Locate and identify every blood parasite.
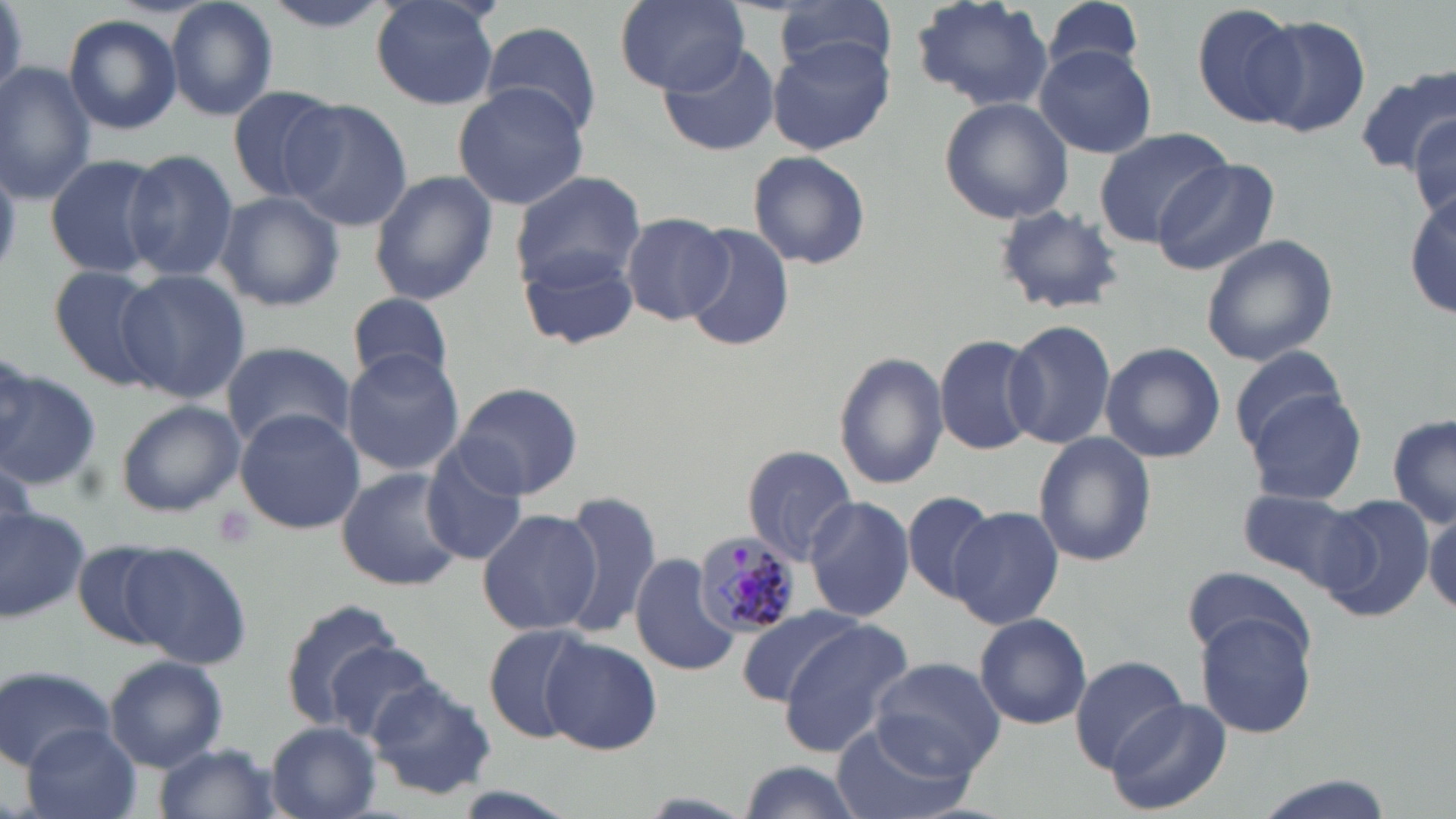

Approximate bounding boxes as named x1/y1/x2/y2 corners in pixels.
Plasmodium malariae-infected red blood cells: (x1=690, y1=529, x2=799, y2=639).
No Plasmodium falciparum, Plasmodium ovale, Plasmodium vivax, Babesia divergens, or Trypanosoma brucei observed.

Uninfected red blood cell locations: (x1=166, y1=0, x2=280, y2=120), (x1=252, y1=0, x2=401, y2=32), (x1=367, y1=0, x2=502, y2=109), (x1=611, y1=0, x2=752, y2=96), (x1=911, y1=0, x2=1053, y2=114), (x1=1038, y1=0, x2=1148, y2=82), (x1=772, y1=1, x2=901, y2=82), (x1=1190, y1=3, x2=1305, y2=128), (x1=64, y1=13, x2=183, y2=135), (x1=1253, y1=15, x2=1374, y2=139), (x1=478, y1=20, x2=604, y2=138), (x1=767, y1=37, x2=893, y2=153), (x1=659, y1=40, x2=782, y2=156), (x1=1035, y1=45, x2=1158, y2=158), (x1=0, y1=62, x2=97, y2=201), (x1=1353, y1=69, x2=1456, y2=181), (x1=452, y1=80, x2=590, y2=211), (x1=224, y1=84, x2=341, y2=203), (x1=280, y1=97, x2=411, y2=230), (x1=939, y1=97, x2=1074, y2=225), (x1=1411, y1=110, x2=1455, y2=221), (x1=1095, y1=127, x2=1231, y2=249), (x1=120, y1=149, x2=239, y2=283), (x1=747, y1=150, x2=871, y2=271), (x1=42, y1=153, x2=166, y2=279), (x1=1152, y1=160, x2=1276, y2=275), (x1=368, y1=170, x2=497, y2=305), (x1=511, y1=171, x2=647, y2=291), (x1=1408, y1=190, x2=1456, y2=321), (x1=214, y1=191, x2=344, y2=312), (x1=993, y1=203, x2=1127, y2=316), (x1=620, y1=212, x2=735, y2=326), (x1=682, y1=224, x2=795, y2=353), (x1=1200, y1=233, x2=1338, y2=366), (x1=519, y1=248, x2=640, y2=350), (x1=47, y1=263, x2=173, y2=393), (x1=118, y1=272, x2=249, y2=405), (x1=346, y1=292, x2=456, y2=384), (x1=1003, y1=318, x2=1117, y2=450), (x1=935, y1=333, x2=1045, y2=456), (x1=221, y1=340, x2=355, y2=450), (x1=1099, y1=341, x2=1226, y2=463), (x1=1228, y1=343, x2=1351, y2=460), (x1=341, y1=349, x2=465, y2=477), (x1=834, y1=350, x2=947, y2=490), (x1=0, y1=367, x2=101, y2=489), (x1=450, y1=381, x2=584, y2=500), (x1=1248, y1=392, x2=1368, y2=505), (x1=113, y1=399, x2=244, y2=517), (x1=233, y1=409, x2=365, y2=534), (x1=1388, y1=412, x2=1456, y2=528), (x1=1033, y1=431, x2=1158, y2=567), (x1=742, y1=445, x2=859, y2=565), (x1=421, y1=447, x2=531, y2=564), (x1=335, y1=467, x2=468, y2=593), (x1=1237, y1=487, x2=1366, y2=589), (x1=556, y1=488, x2=662, y2=640), (x1=900, y1=489, x2=998, y2=604), (x1=804, y1=495, x2=914, y2=623), (x1=1316, y1=495, x2=1434, y2=622), (x1=0, y1=504, x2=90, y2=624), (x1=949, y1=505, x2=1064, y2=629), (x1=476, y1=506, x2=599, y2=636), (x1=1425, y1=509, x2=1456, y2=615), (x1=71, y1=541, x2=183, y2=653), (x1=120, y1=543, x2=254, y2=671), (x1=629, y1=552, x2=736, y2=675), (x1=1187, y1=566, x2=1309, y2=661), (x1=278, y1=596, x2=403, y2=729), (x1=732, y1=607, x2=861, y2=709), (x1=1191, y1=609, x2=1319, y2=739), (x1=973, y1=612, x2=1093, y2=730), (x1=776, y1=620, x2=914, y2=756), (x1=482, y1=625, x2=591, y2=744), (x1=541, y1=634, x2=663, y2=755), (x1=325, y1=643, x2=439, y2=744), (x1=1070, y1=653, x2=1188, y2=771), (x1=106, y1=654, x2=227, y2=770), (x1=869, y1=657, x2=1008, y2=777), (x1=0, y1=664, x2=117, y2=771), (x1=364, y1=680, x2=497, y2=802), (x1=1106, y1=697, x2=1232, y2=816), (x1=829, y1=719, x2=974, y2=819), (x1=24, y1=723, x2=141, y2=819), (x1=265, y1=723, x2=382, y2=818), (x1=150, y1=743, x2=285, y2=819), (x1=734, y1=760, x2=870, y2=819), (x1=1247, y1=773, x2=1398, y2=819). Platelet locations: (x1=210, y1=504, x2=257, y2=550). Slide-level diagnosis: Plasmodium malariae. Image is 1456×819 pixels. Optical microscopy. One field of a larger specimen. Thin blood film. 1000x magnification. May-Grünwald-Giemsa stain.